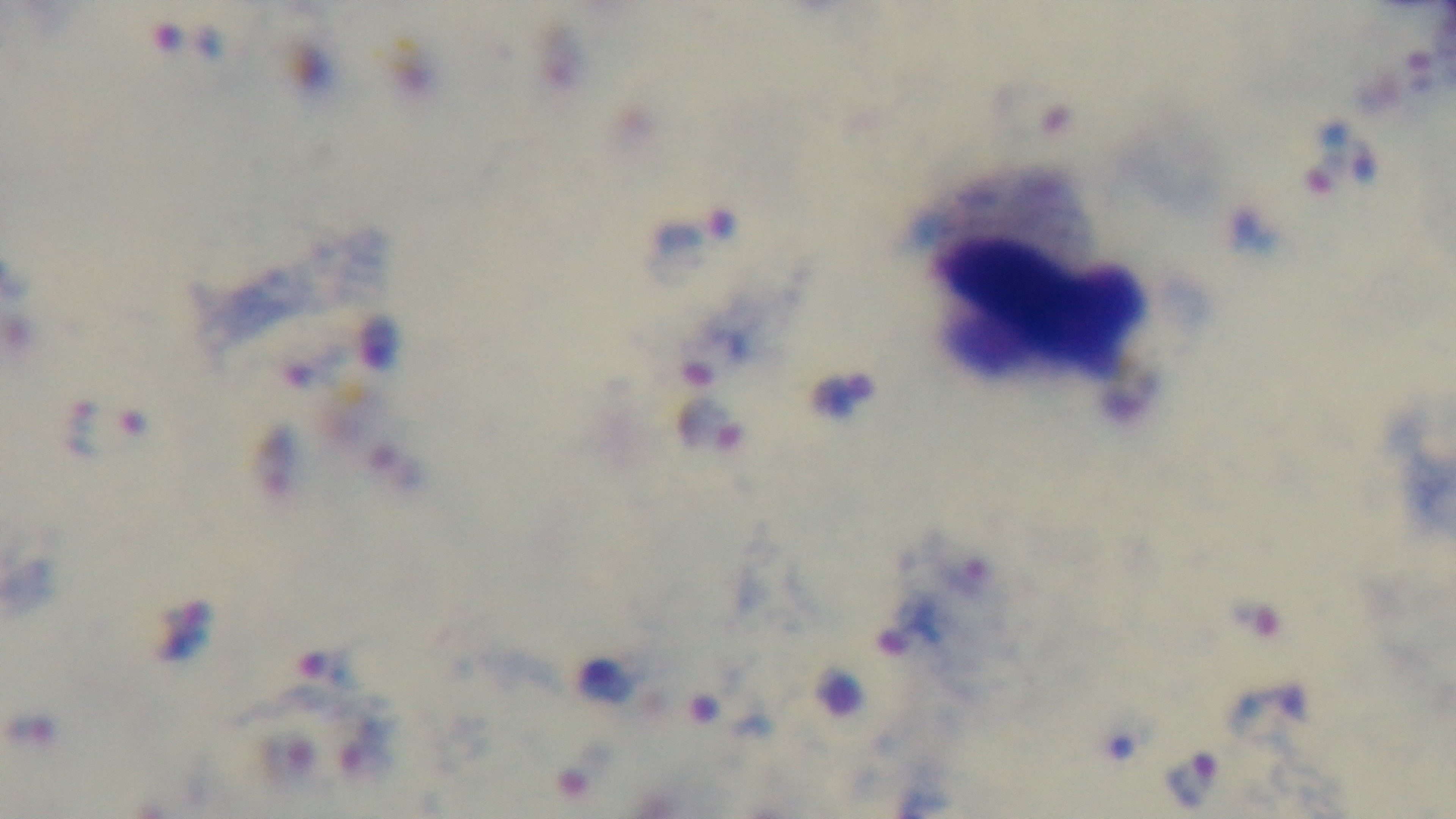
field of view = single
objective = 100x oil immersion
malaria status = infected
capture = mounted 4K digital camera
modality = light microscopy
preparation = thick
stain = Giemsa